Assess this cell for malaria.
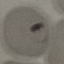

It is parasitized.

Summary:
  - Image type: cell patch, automatically extracted from a larger field of view and resized to 64 × 64 pixels
  - Stain: Giemsa
  - Capture: smartphone through the microscope eyepiece
  - Preparation: thin blood film